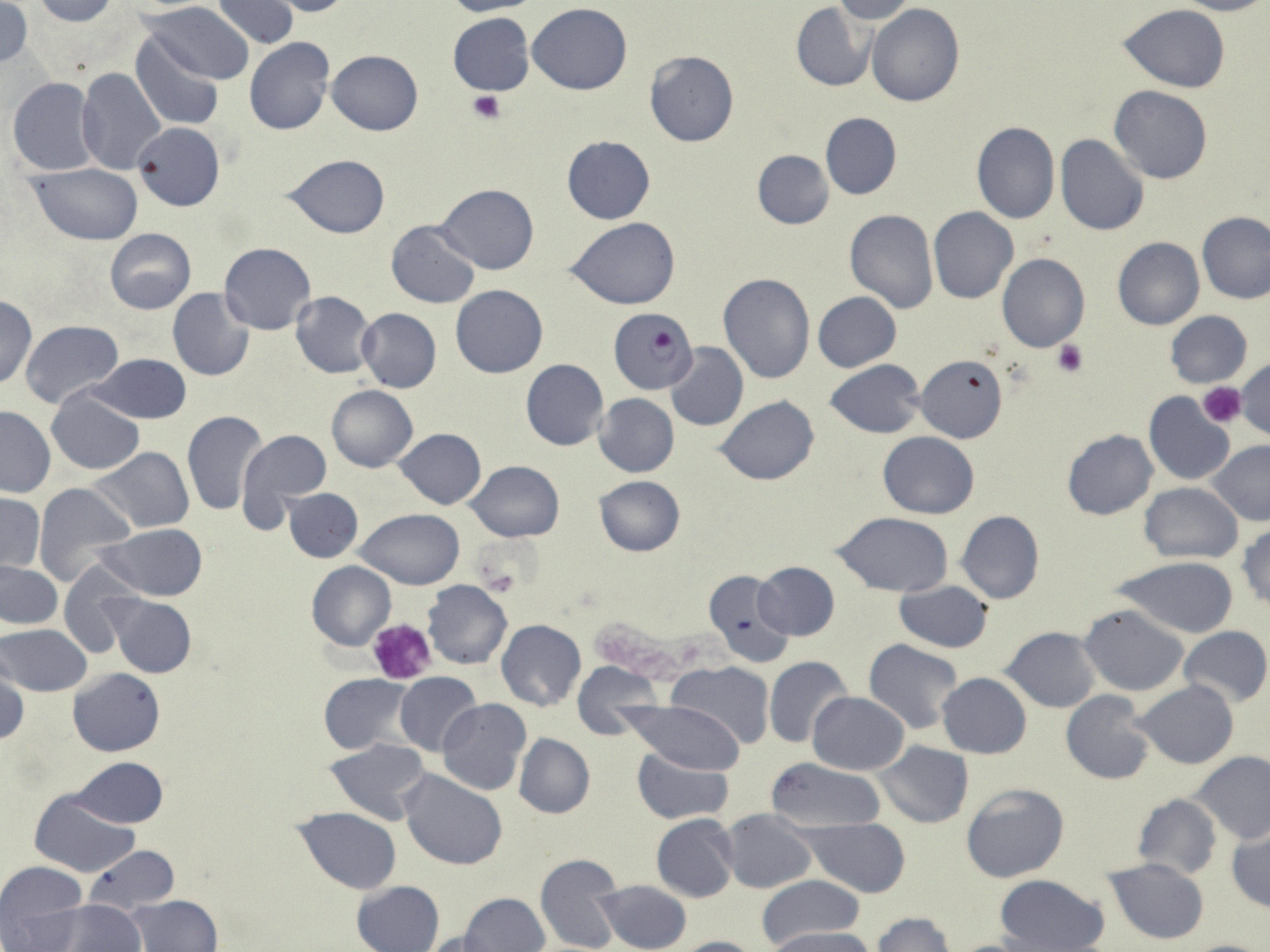
slide-level diagnosis = Plasmodium falciparum
platelet locations = approximate bounding boxes as [x1, y1, x2, y2] in pixels: [468, 90, 506, 123], [1053, 341, 1087, 377], [1198, 383, 1245, 427], [478, 568, 520, 597], [367, 616, 437, 687]
uninfected red blood cell locations = approximate bounding boxes as [x1, y1, x2, y2] in pixels: [30, 0, 118, 25], [211, 0, 299, 48], [262, 0, 355, 17], [439, 0, 542, 16], [834, 0, 918, 24], [1179, 0, 1268, 16], [0, 2, 33, 68], [141, 2, 256, 85], [791, 2, 875, 91], [528, 3, 632, 94], [1118, 3, 1228, 93], [866, 4, 964, 106], [448, 12, 534, 96], [131, 32, 225, 131], [245, 37, 336, 135], [326, 50, 423, 135], [643, 51, 740, 147], [76, 67, 167, 174], [8, 77, 103, 177], [1109, 86, 1214, 184], [820, 112, 901, 199], [134, 121, 224, 212], [971, 121, 1061, 223], [562, 135, 655, 224], [1054, 135, 1149, 237], [752, 151, 834, 229], [282, 154, 389, 238], [30, 164, 144, 244], [434, 183, 539, 274], [928, 208, 1018, 306], [845, 209, 939, 313], [1197, 213, 1269, 304], [567, 217, 680, 309], [386, 221, 480, 309], [104, 228, 196, 314], [1112, 238, 1205, 330], [218, 242, 316, 334], [997, 254, 1090, 353], [719, 273, 814, 384], [450, 285, 548, 378], [167, 288, 256, 382], [289, 291, 378, 378], [813, 291, 901, 372], [1, 295, 38, 388], [356, 308, 442, 392], [1166, 310, 1253, 388], [20, 320, 124, 409], [666, 342, 748, 431], [88, 354, 191, 424], [917, 356, 1007, 442], [1235, 358, 1270, 439], [520, 359, 608, 450], [824, 359, 925, 437], [326, 384, 418, 471], [47, 388, 145, 475], [1143, 392, 1236, 485], [593, 393, 679, 477], [716, 395, 820, 486], [0, 406, 54, 498], [180, 410, 268, 517], [237, 427, 332, 525], [394, 428, 486, 510], [1062, 429, 1158, 519], [878, 431, 980, 518], [1206, 440, 1269, 526], [92, 447, 195, 534], [465, 460, 564, 542], [594, 476, 685, 557], [1140, 482, 1242, 564], [33, 483, 135, 587], [283, 488, 363, 563], [0, 492, 44, 573], [354, 509, 464, 589], [956, 510, 1045, 605], [831, 511, 954, 596], [97, 524, 208, 601], [1238, 524, 1270, 609], [1110, 557, 1240, 639], [57, 558, 144, 660], [306, 560, 396, 651], [0, 561, 62, 628], [756, 562, 840, 639], [702, 569, 812, 669], [894, 579, 993, 652], [423, 580, 511, 670], [107, 595, 197, 679], [1079, 604, 1189, 695], [495, 620, 587, 710], [0, 625, 90, 696], [1001, 625, 1103, 713], [1177, 626, 1270, 708], [863, 639, 966, 735], [763, 657, 855, 748], [573, 660, 662, 737], [668, 661, 773, 745], [1, 663, 28, 747], [68, 669, 165, 756], [394, 671, 484, 757], [318, 673, 416, 754], [937, 673, 1032, 757], [1134, 680, 1239, 768], [1060, 690, 1157, 785], [807, 691, 911, 774], [437, 699, 530, 796], [623, 700, 747, 773], [512, 733, 596, 819], [326, 738, 431, 825], [873, 741, 973, 828], [631, 748, 734, 824], [1190, 750, 1270, 844], [72, 756, 169, 828], [764, 757, 888, 833], [399, 769, 507, 870], [960, 780, 1071, 883], [30, 790, 140, 878], [1133, 794, 1222, 879], [292, 808, 402, 894], [721, 809, 819, 893], [651, 813, 740, 903], [801, 817, 911, 897], [1227, 821, 1269, 914], [83, 846, 180, 915], [534, 853, 623, 952], [1103, 857, 1210, 945], [0, 860, 88, 944], [994, 874, 1111, 952], [756, 875, 863, 950], [594, 879, 692, 952], [352, 880, 445, 952], [458, 892, 551, 952], [126, 894, 221, 952], [37, 900, 145, 950], [872, 913, 958, 952], [765, 927, 876, 952], [416, 930, 507, 952], [671, 936, 763, 952], [944, 937, 1045, 952], [1179, 938, 1269, 952]
stain = May-Grünwald-Giemsa
magnification = 1000x
Plasmodium falciparum-infected red blood cell locations = approximate bounding boxes as [x1, y1, x2, y2] in pixels: [609, 308, 699, 393]
image size = 1270×952 pixels
field of view = single
modality = light microscopy
preparation = thin blood smear